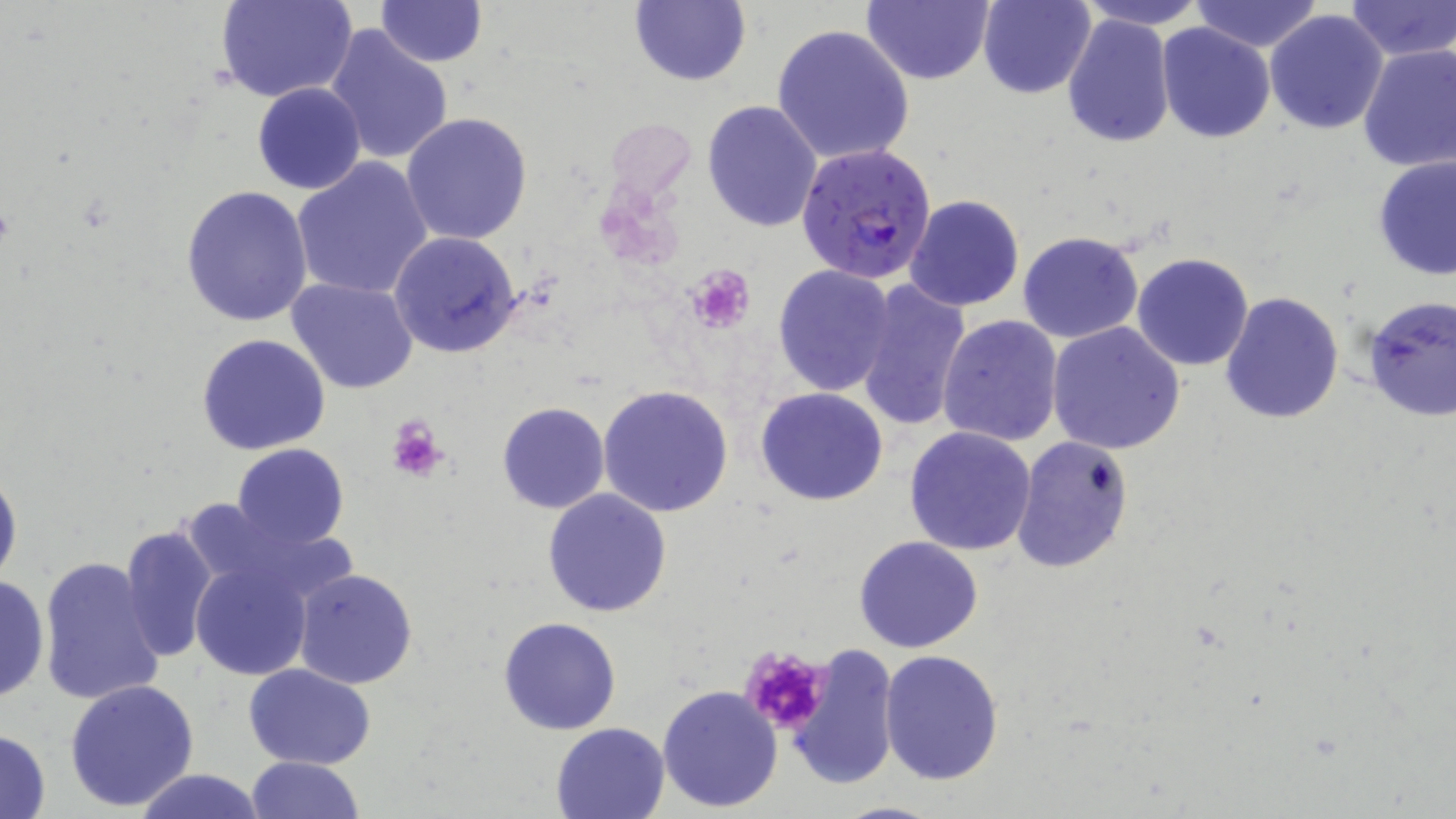

Approximate bounding boxes as (x1, y1, x2, y2) in pixels. Uninfected red blood cell locations: (215, 0, 356, 104), (629, 0, 749, 86), (1077, 0, 1208, 30), (1189, 0, 1326, 52), (1345, 0, 1455, 61), (377, 1, 487, 67), (862, 1, 995, 86), (978, 1, 1095, 99), (1265, 9, 1389, 134), (1061, 14, 1175, 150), (1156, 22, 1275, 142), (772, 24, 915, 165), (325, 26, 453, 165), (1357, 42, 1456, 172), (253, 82, 367, 195), (701, 99, 823, 232), (401, 113, 533, 245), (1372, 155, 1456, 280), (292, 157, 433, 299), (180, 184, 314, 327), (904, 195, 1025, 312), (389, 230, 523, 359), (1017, 231, 1145, 344), (1132, 253, 1253, 371), (772, 264, 896, 397), (287, 278, 418, 394), (855, 278, 973, 432), (1220, 293, 1345, 425), (1358, 295, 1456, 425), (937, 314, 1063, 448), (1046, 322, 1186, 454), (195, 334, 332, 457), (596, 385, 736, 518), (755, 386, 889, 506), (497, 401, 610, 514), (905, 425, 1037, 556), (1010, 437, 1135, 574), (231, 443, 350, 550), (0, 466, 22, 595), (542, 489, 672, 617), (120, 524, 219, 662), (854, 536, 984, 655), (188, 554, 321, 682), (38, 556, 167, 708), (293, 568, 418, 690), (0, 573, 50, 706), (497, 616, 620, 734), (788, 643, 899, 790), (880, 648, 1004, 785), (244, 664, 375, 770), (65, 678, 200, 813), (657, 684, 784, 813), (552, 721, 670, 818), (0, 728, 52, 818), (244, 755, 364, 818), (133, 768, 266, 819), (829, 799, 945, 818). Plasmodium falciparum-infected red blood cell locations: (793, 142, 937, 283). Platelet locations: (687, 263, 754, 332), (385, 414, 449, 484), (740, 646, 832, 733). Slide-level diagnosis: Plasmodium falciparum. Image is 1456×819 pixels. Optical microscopy. May-Grünwald-Giemsa stain. Captured at 1000x magnification. Thin blood film. Single field of view.